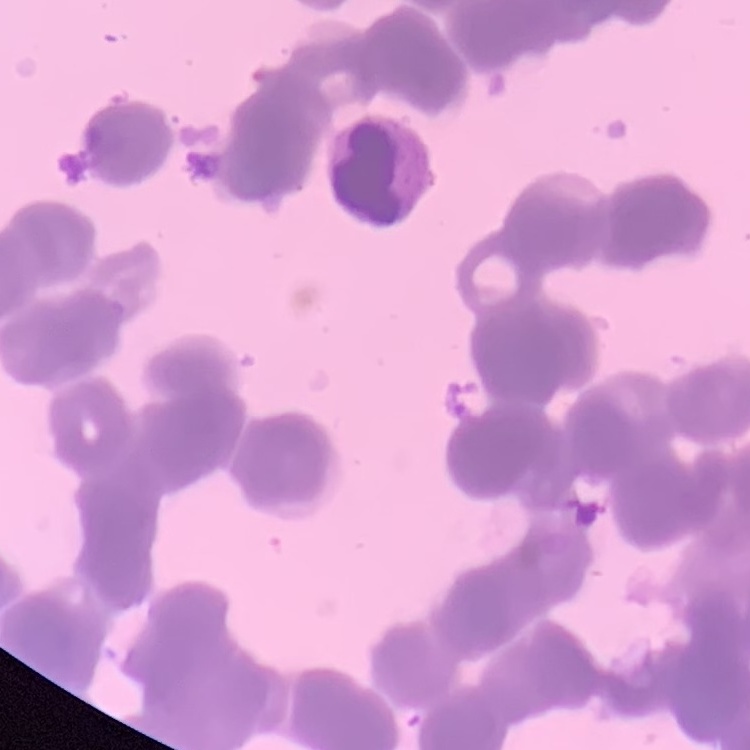
erythrocyte morphology = rouleaux formation
stain = Field's or Giemsa
preparation = thin peripheral smear
image type = one tile cut from a larger photomicrograph